State the blood parasite species.
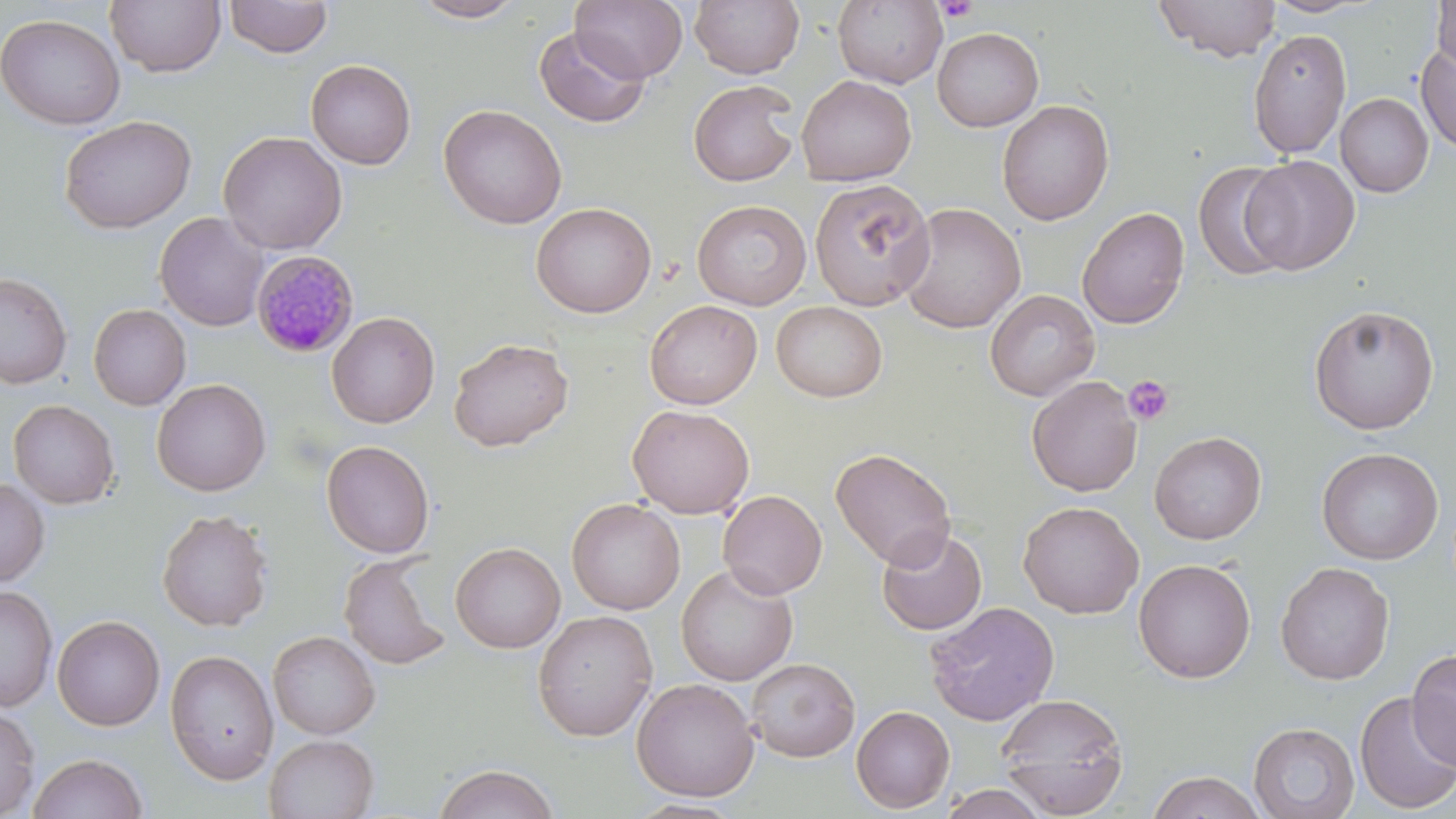

Plasmodium malariae.

{
  "magnification": "1000x",
  "plasmodium_malariae_infected_red_blood_cell_locations": "approximate bounding boxes as [x1, y1, x2, y2] in pixels: [249, 248, 359, 358]",
  "uninfected_red_blood_cell_locations": "approximate bounding boxes as [x1, y1, x2, y2] in pixels: [409, 0, 528, 23], [570, 0, 690, 84], [690, 0, 804, 79], [833, 0, 947, 88], [1155, 0, 1281, 62], [1263, 0, 1375, 18], [105, 1, 226, 78], [224, 1, 333, 59], [1431, 1, 1456, 79], [0, 13, 125, 129], [534, 26, 650, 128], [932, 27, 1044, 131], [1247, 28, 1352, 158], [1415, 41, 1456, 154], [306, 59, 416, 170], [796, 74, 917, 186], [688, 80, 800, 187], [1336, 93, 1433, 198], [996, 100, 1114, 226], [438, 104, 567, 230], [58, 115, 196, 234], [218, 131, 347, 255], [1240, 156, 1360, 275], [1191, 161, 1297, 282], [809, 177, 937, 310], [692, 199, 812, 310], [531, 202, 656, 318], [897, 203, 1026, 333], [1077, 206, 1190, 329], [155, 212, 269, 332], [0, 271, 72, 388], [984, 289, 1100, 401], [644, 300, 762, 409], [771, 301, 887, 402], [88, 304, 191, 410], [1309, 304, 1439, 434], [326, 311, 440, 428], [449, 337, 573, 451], [1026, 375, 1143, 497], [152, 378, 271, 496], [8, 399, 119, 509], [628, 404, 754, 519], [1149, 431, 1267, 545], [321, 440, 435, 558], [830, 447, 957, 571], [1316, 447, 1443, 564], [0, 477, 50, 587], [717, 490, 827, 599], [566, 498, 685, 615], [1018, 501, 1144, 619], [155, 509, 274, 632], [876, 526, 988, 636], [450, 542, 565, 653], [340, 553, 451, 670], [1133, 558, 1256, 683], [1275, 561, 1395, 685], [676, 563, 798, 686], [1, 585, 58, 712], [923, 601, 1060, 727], [532, 609, 658, 742], [52, 615, 165, 731], [268, 631, 381, 740], [1406, 648, 1456, 770], [165, 649, 279, 785], [746, 657, 860, 762], [631, 678, 760, 801], [1354, 692, 1456, 815], [996, 693, 1128, 816], [851, 705, 956, 813], [0, 706, 40, 819], [1248, 722, 1359, 819], [263, 734, 378, 818], [27, 752, 148, 819], [434, 763, 560, 819], [1146, 771, 1267, 819], [939, 784, 1050, 819], [626, 797, 746, 818]",
  "modality": "optical microscopy",
  "preparation": "thin blood smear",
  "platelet_locations": "approximate bounding boxes as [x1, y1, x2, y2] in pixels: [934, 0, 978, 22], [1124, 376, 1173, 424]",
  "image_size": "1456×819 pixels",
  "field_of_view": "single",
  "stain": "May-Grünwald-Giemsa"
}